Outline each blood parasite and name the species.
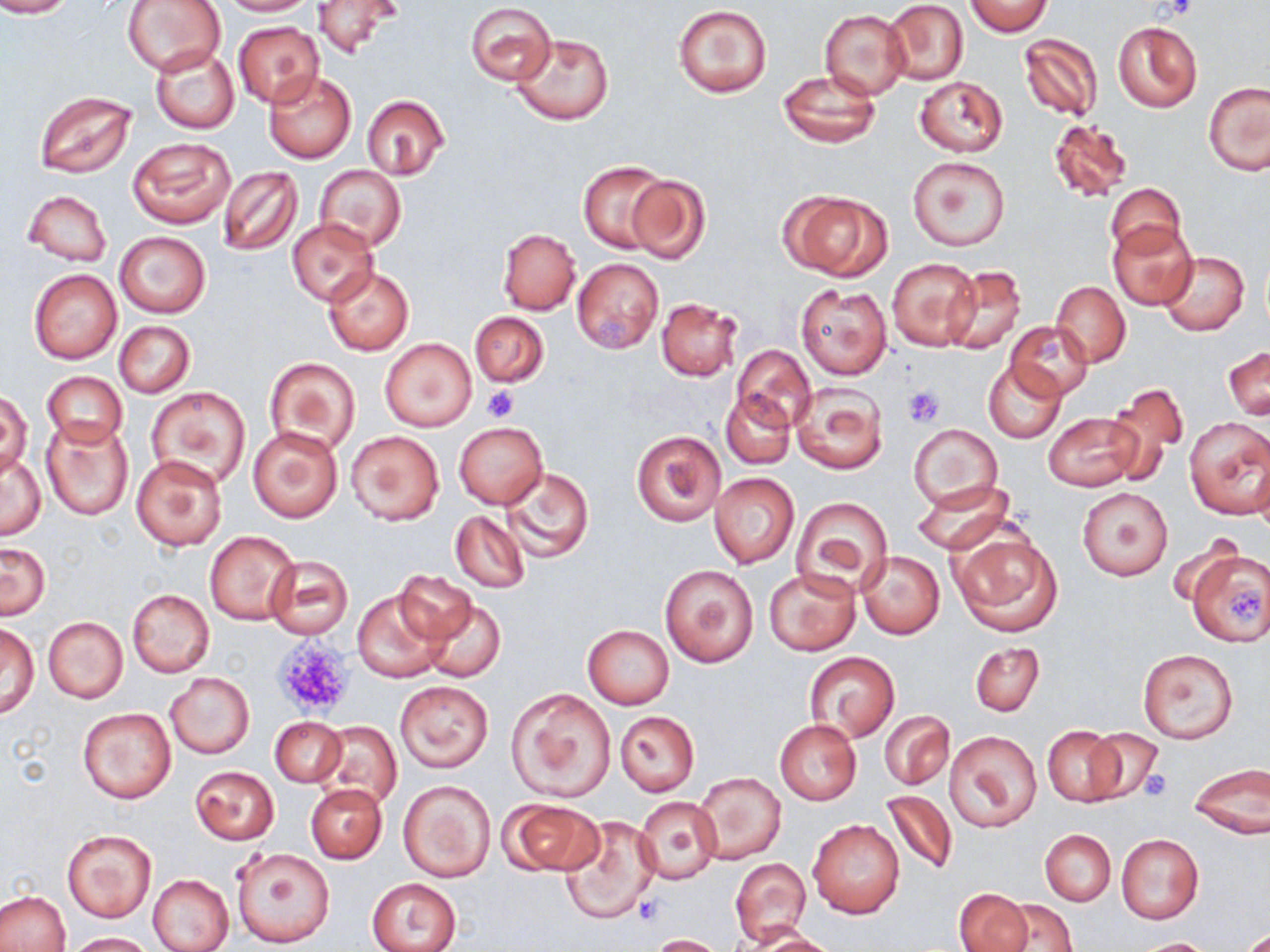
No blood parasites observed.

Approximate bounding boxes as named x1/y1/x2/y2 corners in pixels. Platelet locations: (x1=1162, y1=0, x2=1198, y2=21), (x1=481, y1=384, x2=520, y2=422), (x1=902, y1=386, x2=946, y2=428), (x1=1228, y1=589, x2=1266, y2=627), (x1=271, y1=634, x2=356, y2=720), (x1=1138, y1=769, x2=1172, y2=801), (x1=633, y1=891, x2=667, y2=925). Uninfected red blood cell locations: (x1=0, y1=0, x2=75, y2=17), (x1=123, y1=0, x2=224, y2=76), (x1=216, y1=0, x2=314, y2=15), (x1=965, y1=0, x2=1052, y2=35), (x1=310, y1=1, x2=401, y2=59), (x1=884, y1=1, x2=968, y2=85), (x1=466, y1=2, x2=556, y2=85), (x1=673, y1=5, x2=773, y2=98), (x1=819, y1=9, x2=910, y2=98), (x1=232, y1=21, x2=324, y2=108), (x1=1113, y1=21, x2=1201, y2=112), (x1=509, y1=32, x2=615, y2=126), (x1=1019, y1=33, x2=1102, y2=122), (x1=150, y1=45, x2=240, y2=134), (x1=263, y1=70, x2=358, y2=163), (x1=777, y1=70, x2=881, y2=148), (x1=914, y1=75, x2=1008, y2=156), (x1=1203, y1=82, x2=1270, y2=175), (x1=33, y1=89, x2=137, y2=179), (x1=361, y1=94, x2=450, y2=181), (x1=1046, y1=117, x2=1134, y2=202), (x1=127, y1=138, x2=234, y2=229), (x1=908, y1=155, x2=1011, y2=252), (x1=577, y1=161, x2=667, y2=254), (x1=315, y1=165, x2=406, y2=250), (x1=216, y1=166, x2=303, y2=256), (x1=625, y1=174, x2=711, y2=264), (x1=1106, y1=182, x2=1186, y2=260), (x1=779, y1=189, x2=891, y2=281), (x1=23, y1=190, x2=112, y2=266), (x1=287, y1=218, x2=378, y2=306), (x1=1108, y1=221, x2=1197, y2=310), (x1=498, y1=229, x2=580, y2=314), (x1=115, y1=231, x2=210, y2=318), (x1=1159, y1=251, x2=1248, y2=336), (x1=886, y1=257, x2=981, y2=352), (x1=572, y1=258, x2=665, y2=354), (x1=943, y1=263, x2=1027, y2=356), (x1=323, y1=267, x2=414, y2=357), (x1=29, y1=270, x2=121, y2=363), (x1=1050, y1=280, x2=1131, y2=366), (x1=797, y1=284, x2=891, y2=379), (x1=656, y1=297, x2=743, y2=382), (x1=470, y1=311, x2=550, y2=387), (x1=1005, y1=320, x2=1093, y2=402), (x1=115, y1=321, x2=195, y2=398), (x1=380, y1=337, x2=478, y2=433), (x1=731, y1=345, x2=815, y2=435), (x1=1224, y1=346, x2=1270, y2=419), (x1=264, y1=357, x2=359, y2=455), (x1=983, y1=361, x2=1066, y2=442), (x1=42, y1=372, x2=127, y2=449), (x1=791, y1=382, x2=889, y2=474), (x1=1105, y1=383, x2=1189, y2=484), (x1=147, y1=386, x2=250, y2=489), (x1=721, y1=390, x2=794, y2=468), (x1=0, y1=391, x2=32, y2=477), (x1=1044, y1=411, x2=1144, y2=492), (x1=1184, y1=417, x2=1270, y2=519), (x1=42, y1=419, x2=133, y2=521), (x1=453, y1=422, x2=548, y2=508), (x1=911, y1=423, x2=1002, y2=512), (x1=248, y1=427, x2=342, y2=522), (x1=630, y1=429, x2=725, y2=527), (x1=346, y1=430, x2=444, y2=524), (x1=2, y1=454, x2=46, y2=539), (x1=131, y1=454, x2=229, y2=551), (x1=500, y1=465, x2=593, y2=562), (x1=710, y1=472, x2=800, y2=568), (x1=910, y1=477, x2=1013, y2=554), (x1=1077, y1=488, x2=1173, y2=580), (x1=792, y1=497, x2=893, y2=595), (x1=450, y1=510, x2=529, y2=593), (x1=950, y1=526, x2=1063, y2=637), (x1=204, y1=530, x2=300, y2=625), (x1=0, y1=542, x2=50, y2=619), (x1=1185, y1=549, x2=1270, y2=647), (x1=857, y1=550, x2=944, y2=640), (x1=266, y1=554, x2=353, y2=639), (x1=659, y1=564, x2=759, y2=667), (x1=765, y1=568, x2=860, y2=656), (x1=395, y1=570, x2=478, y2=647), (x1=352, y1=588, x2=447, y2=681), (x1=127, y1=590, x2=214, y2=676), (x1=420, y1=598, x2=505, y2=684), (x1=42, y1=616, x2=128, y2=704), (x1=1, y1=624, x2=39, y2=719), (x1=583, y1=624, x2=674, y2=709), (x1=969, y1=641, x2=1045, y2=716), (x1=1137, y1=649, x2=1238, y2=743), (x1=804, y1=653, x2=899, y2=742), (x1=166, y1=673, x2=254, y2=757), (x1=394, y1=681, x2=494, y2=772), (x1=506, y1=688, x2=616, y2=802), (x1=77, y1=708, x2=175, y2=805), (x1=615, y1=710, x2=700, y2=794), (x1=881, y1=711, x2=954, y2=790), (x1=270, y1=717, x2=346, y2=787), (x1=774, y1=718, x2=861, y2=806), (x1=316, y1=721, x2=402, y2=812), (x1=1042, y1=725, x2=1123, y2=805), (x1=1085, y1=727, x2=1164, y2=805), (x1=946, y1=730, x2=1041, y2=832), (x1=1188, y1=762, x2=1270, y2=838), (x1=190, y1=766, x2=279, y2=845), (x1=694, y1=772, x2=785, y2=863), (x1=398, y1=779, x2=495, y2=883), (x1=304, y1=783, x2=385, y2=863), (x1=880, y1=789, x2=959, y2=877), (x1=634, y1=797, x2=723, y2=883), (x1=500, y1=798, x2=604, y2=877), (x1=559, y1=814, x2=660, y2=925), (x1=808, y1=819, x2=905, y2=918), (x1=63, y1=829, x2=155, y2=922), (x1=1040, y1=829, x2=1114, y2=905), (x1=1115, y1=834, x2=1205, y2=924), (x1=232, y1=846, x2=335, y2=947), (x1=730, y1=857, x2=811, y2=946), (x1=148, y1=874, x2=235, y2=952), (x1=367, y1=878, x2=461, y2=952), (x1=954, y1=889, x2=1034, y2=952), (x1=0, y1=891, x2=70, y2=952), (x1=999, y1=899, x2=1077, y2=951), (x1=1241, y1=926, x2=1270, y2=951), (x1=746, y1=928, x2=840, y2=951), (x1=70, y1=932, x2=157, y2=951), (x1=649, y1=934, x2=729, y2=952), (x1=1133, y1=938, x2=1217, y2=951). Slide-level diagnosis: no evidence of blood parasites. Thin blood film. Image is 1270×952 pixels. 1000x magnification. Light microscopy. One field of a larger specimen. May-Grünwald-Giemsa stain.